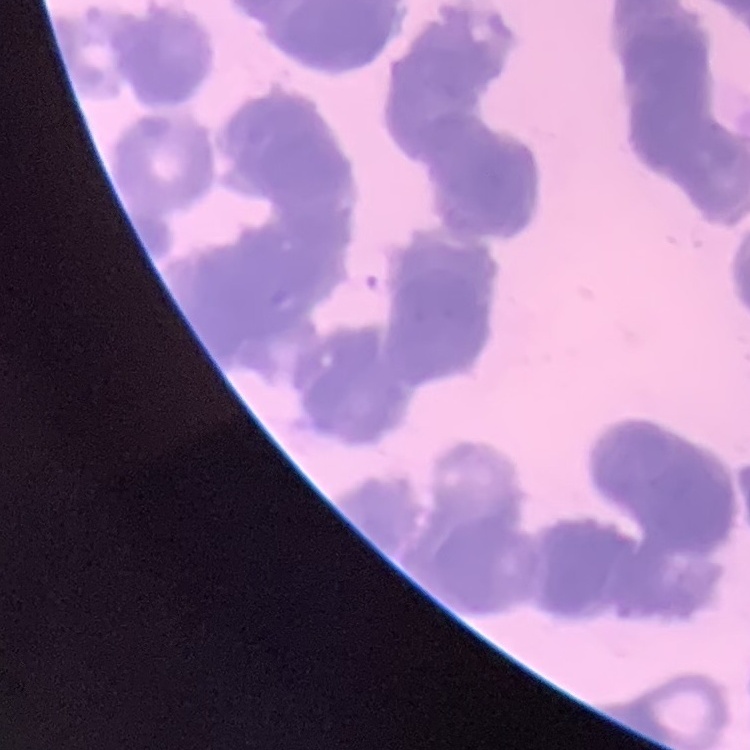

Summary:
  - Erythrocyte morphology: rouleaux formation
  - Image type: square crop of a larger photomicrograph
  - Preparation: thin blood smear
  - Stain: Field's or Giemsa